Outline each blood parasite and name the species.
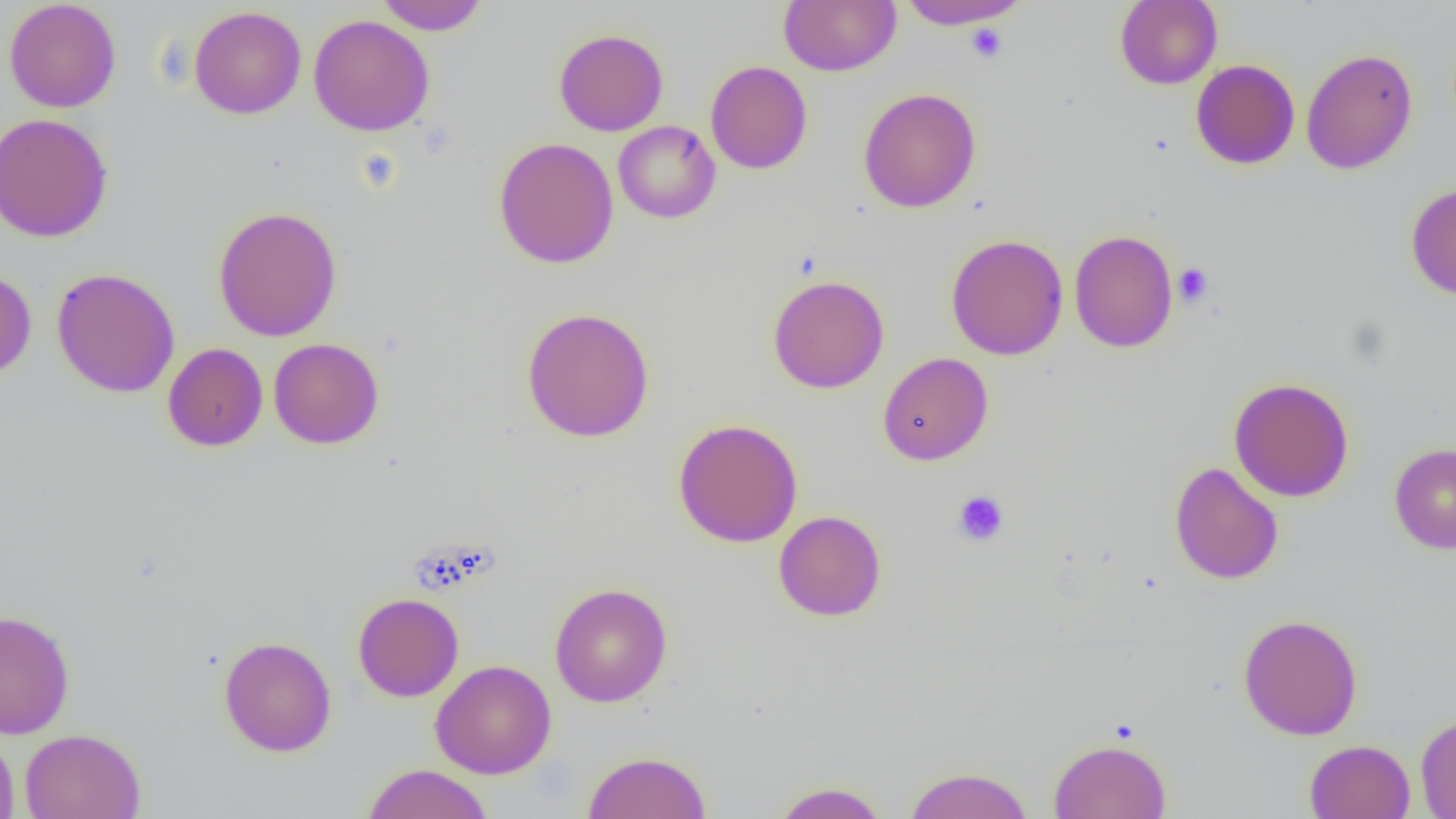

No blood parasites seen.

Summary:
  - Coordinate format: approximate bounding boxes as (x1,y1)-(x2,y2) corner pairs in pixels
  - Platelet locations: (965,23)-(1008,63), (1173,263)-(1214,307), (952,490)-(1010,546)
  - Uninfected red blood cell locations: (4,0)-(122,113), (375,0)-(490,35), (779,0)-(900,76), (896,0)-(1031,30), (1114,0)-(1222,89), (189,6)-(307,119), (308,14)-(435,136), (959,20)-(1017,62), (554,28)-(668,136), (1301,49)-(1417,174), (1191,59)-(1300,169), (706,61)-(812,174), (858,87)-(981,213), (0,112)-(113,242), (613,121)-(721,224), (493,137)-(619,269), (1405,182)-(1456,299), (212,206)-(343,342), (1069,229)-(1178,353), (946,234)-(1068,360), (0,268)-(37,380), (52,268)-(180,398), (767,274)-(889,394), (520,307)-(655,443), (268,338)-(384,449), (163,343)-(268,451), (878,352)-(993,466), (1229,377)-(1354,502), (673,418)-(803,548), (1389,443)-(1456,554), (1169,462)-(1284,584), (773,510)-(887,622), (549,582)-(673,707), (352,592)-(464,702), (0,609)-(75,739), (1237,613)-(1363,740), (218,636)-(337,757), (430,659)-(556,779), (1415,714)-(1456,817), (0,726)-(20,819), (20,729)-(145,819), (1048,738)-(1171,818), (1305,740)-(1415,819), (582,750)-(712,819), (361,763)-(493,819), (902,766)-(1035,819), (770,781)-(890,819)
  - Slide-level diagnosis: no evidence of blood parasites
  - Modality: optical microscopy
  - Preparation: thin blood smear
  - Image size: 1456×819 pixels
  - Field of view: one of a larger specimen
  - Magnification: 1000x